Report the malaria status of this cell.
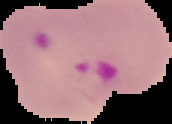
Parasitized.

image type = cell region segmented out of the field of view; surrounding area masked to black
image size = 172×124 pixels
preparation = thin blood film